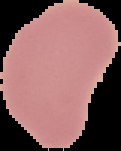 Cell region segmented out of the field of view; the surrounding area is masked to black. From a thin blood smear. Malaria status: uninfected. Image is 121×151 pixels.